Describe the morphology of the erythrocytes.
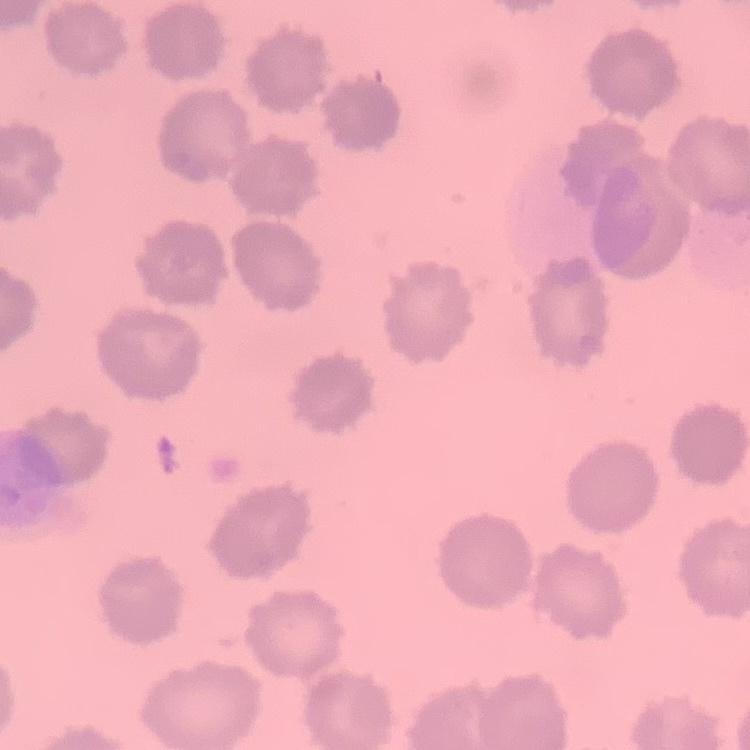

They show no rouleaux formation.

Summary:
  - Image type: one tile cut from a larger photomicrograph
  - Preparation: thin blood film
  - Stain: Field's or Giemsa